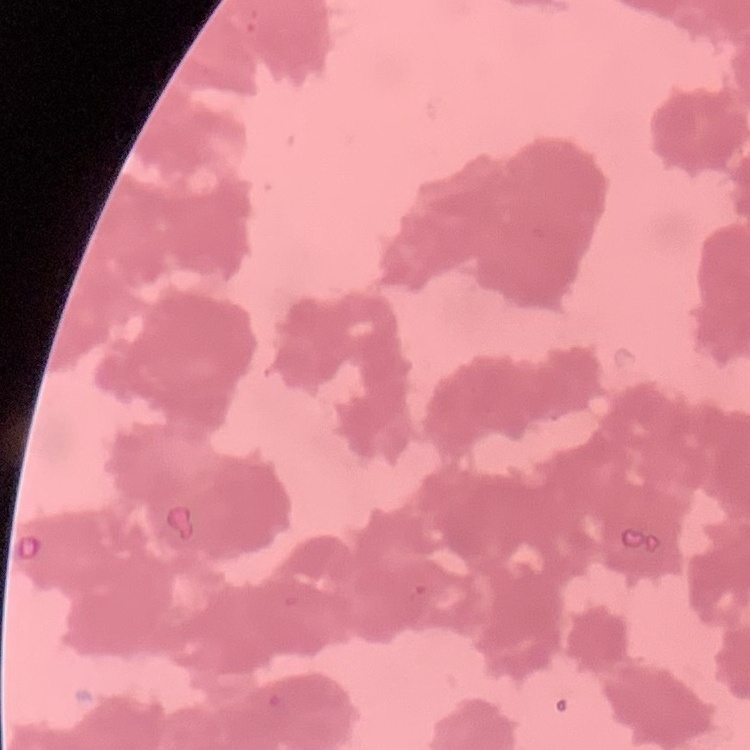
Summary:
  - Red blood cell morphology: rouleaux formation
  - Preparation: thin peripheral smear
  - Image type: one tile cut from a larger photomicrograph
  - Stain: Field's or Giemsa